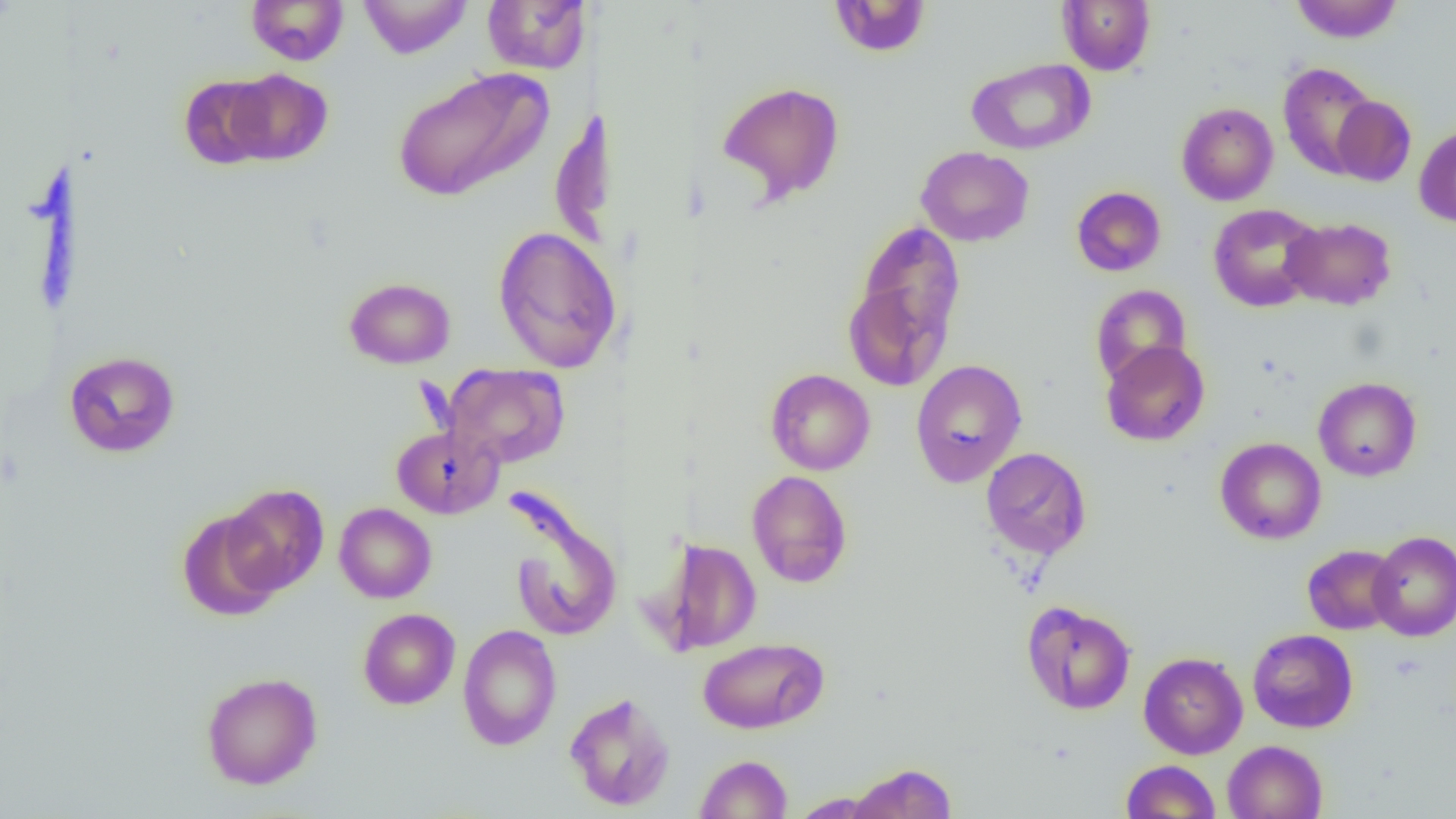
Summary:
  - Coordinate format: approximate bounding boxes as named x1/y1/x2/y2 corners in pixels
  - Uninfected red blood cell locations: (x1=358, y1=0, x2=472, y2=59), (x1=482, y1=0, x2=590, y2=74), (x1=829, y1=0, x2=931, y2=57), (x1=1057, y1=0, x2=1155, y2=75), (x1=1290, y1=0, x2=1402, y2=43), (x1=246, y1=1, x2=349, y2=65), (x1=966, y1=58, x2=1096, y2=155), (x1=1278, y1=62, x2=1379, y2=179), (x1=392, y1=66, x2=554, y2=202), (x1=226, y1=68, x2=333, y2=166), (x1=178, y1=75, x2=276, y2=169), (x1=717, y1=81, x2=845, y2=204), (x1=1178, y1=94, x2=1381, y2=192), (x1=1331, y1=95, x2=1416, y2=186), (x1=551, y1=102, x2=609, y2=256), (x1=1176, y1=102, x2=1278, y2=206), (x1=1414, y1=124, x2=1456, y2=227), (x1=915, y1=146, x2=1034, y2=246), (x1=1071, y1=186, x2=1166, y2=276), (x1=1208, y1=203, x2=1323, y2=312), (x1=1281, y1=216, x2=1396, y2=311), (x1=846, y1=224, x2=965, y2=389), (x1=492, y1=225, x2=622, y2=374), (x1=344, y1=277, x2=456, y2=369), (x1=1090, y1=284, x2=1192, y2=387), (x1=1101, y1=341, x2=1210, y2=446), (x1=64, y1=351, x2=180, y2=458), (x1=911, y1=359, x2=1027, y2=487), (x1=443, y1=363, x2=570, y2=468), (x1=765, y1=368, x2=875, y2=475), (x1=1313, y1=377, x2=1422, y2=482), (x1=391, y1=424, x2=502, y2=519), (x1=1215, y1=437, x2=1327, y2=544), (x1=981, y1=447, x2=1091, y2=559), (x1=747, y1=470, x2=853, y2=588), (x1=222, y1=484, x2=329, y2=595), (x1=502, y1=485, x2=622, y2=642), (x1=334, y1=503, x2=436, y2=603), (x1=177, y1=508, x2=284, y2=621), (x1=1368, y1=530, x2=1456, y2=642), (x1=660, y1=539, x2=762, y2=654), (x1=1302, y1=544, x2=1401, y2=635), (x1=1022, y1=601, x2=1136, y2=715), (x1=358, y1=608, x2=460, y2=709), (x1=458, y1=624, x2=562, y2=751), (x1=1247, y1=629, x2=1358, y2=733), (x1=697, y1=637, x2=828, y2=734), (x1=1138, y1=652, x2=1248, y2=759), (x1=201, y1=672, x2=323, y2=789), (x1=564, y1=691, x2=676, y2=811), (x1=1222, y1=740, x2=1327, y2=818), (x1=694, y1=754, x2=793, y2=818), (x1=1121, y1=760, x2=1221, y2=818), (x1=847, y1=762, x2=957, y2=818), (x1=789, y1=792, x2=886, y2=817)
  - Slide-level diagnosis: no evidence of blood parasites
  - Image size: 1456×819 pixels
  - Field of view: one of a larger specimen
  - Modality: optical microscopy
  - Preparation: thin blood smear
  - Magnification: 1000x